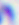
Micrograph. Toxoplasma gondii is shown. 400x magnification.